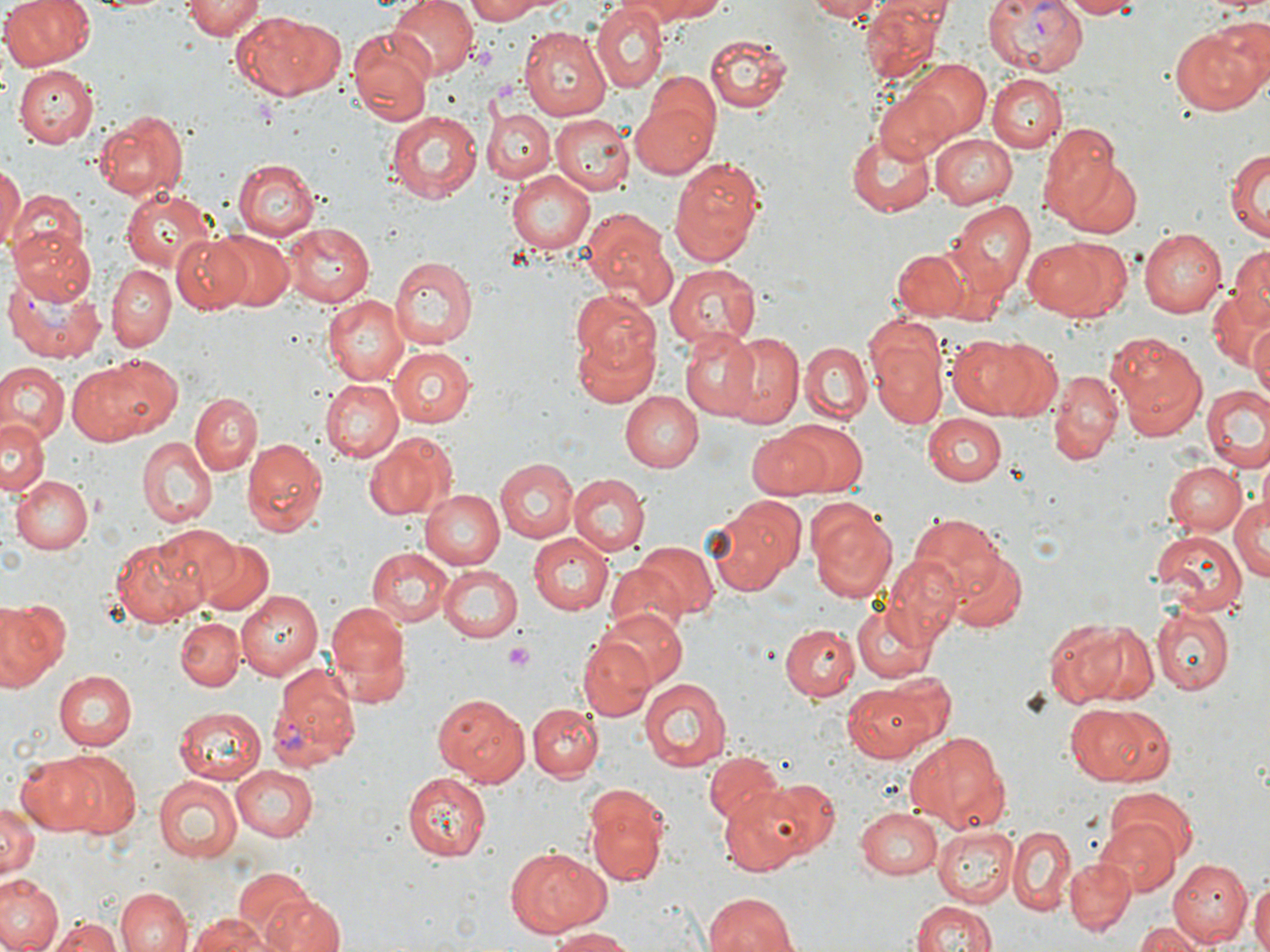
slide-level diagnosis = Plasmodium vivax
platelet locations = approximate bounding boxes as (x1,y1)-(x2,y2) corner pairs in pixels: (471,47)-(496,70), (505,643)-(536,671)
image size = 1270×952 pixels
magnification = 1000x
preparation = thin blood film
stain = May-Grünwald-Giemsa
Plasmodium vivax-infected red blood cell locations = approximate bounding boxes as (x1,y1)-(x2,y2) corner pairs in pixels: (981,0)-(1090,75), (4,269)-(105,363), (265,671)-(362,775)
field of view = one of a larger specimen
modality = optical microscopy
uninfected red blood cell locations = approximate bounding boxes as (x1,y1)-(x2,y2) corner pairs in pixels: (1,0)-(95,70), (179,0)-(263,38), (387,0)-(474,80), (462,0)-(549,24), (615,0)-(726,31), (803,0)-(885,21), (1058,0)-(1142,17), (862,1)-(950,78), (590,5)-(666,89), (230,9)-(345,99), (540,11)-(658,131), (1170,21)-(1267,114), (519,26)-(612,120), (347,29)-(435,127), (704,33)-(791,114), (634,55)-(747,156), (903,59)-(991,142), (12,64)-(98,146), (988,73)-(1065,151), (871,84)-(965,166), (629,93)-(718,178), (483,108)-(554,182), (93,109)-(188,201), (385,112)-(481,203), (551,115)-(633,196), (1039,121)-(1125,224), (847,132)-(936,216), (931,132)-(1018,209), (1224,148)-(1269,242), (1061,156)-(1143,238), (668,159)-(768,267), (0,160)-(23,250), (234,160)-(319,240), (506,170)-(594,254), (120,188)-(216,273), (7,190)-(89,275), (947,201)-(1036,297), (581,209)-(678,311), (283,222)-(374,306), (11,227)-(97,307), (1138,229)-(1226,317), (210,230)-(294,310), (173,232)-(257,315), (1021,238)-(1130,323), (1229,244)-(1270,323), (891,248)-(970,321), (391,257)-(478,349), (104,265)-(174,352), (665,265)-(762,348), (1205,285)-(1267,374), (571,288)-(659,380), (324,296)-(408,387), (1249,323)-(1270,404), (573,327)-(659,408), (679,329)-(764,421), (868,331)-(950,427), (946,332)-(1056,419), (721,333)-(803,425), (1104,333)-(1207,438), (800,341)-(872,423), (390,347)-(475,427), (67,355)-(174,446), (2,362)-(68,444), (1049,372)-(1122,461), (318,378)-(402,462), (1202,385)-(1269,472), (621,391)-(701,472), (191,392)-(262,475), (922,414)-(1005,486), (0,419)-(46,498), (782,422)-(867,494), (746,427)-(832,498), (363,431)-(459,520), (136,437)-(218,529), (243,437)-(328,537), (495,459)-(577,543), (1165,461)-(1246,535), (568,474)-(649,557), (11,475)-(93,554), (423,489)-(505,570), (1230,491)-(1270,585), (703,495)-(804,595), (806,498)-(898,604), (907,510)-(1010,602), (152,525)-(242,605), (529,531)-(614,615), (1152,531)-(1244,616), (111,535)-(205,626), (195,539)-(272,615), (631,541)-(720,621), (367,546)-(451,627), (945,548)-(1026,631), (887,557)-(965,641), (604,561)-(691,639), (438,565)-(524,643), (235,590)-(324,678), (0,596)-(71,692), (853,602)-(940,685), (328,603)-(411,686), (599,606)-(688,689), (1152,608)-(1233,694), (1048,615)-(1157,706), (175,617)-(245,693), (779,623)-(858,701), (580,636)-(653,719), (52,669)-(136,748), (639,677)-(732,773), (845,681)-(945,762), (434,691)-(530,788), (528,702)-(604,779), (1062,702)-(1166,785), (174,706)-(266,783), (907,730)-(1010,832), (706,752)-(786,828), (16,753)-(107,837), (59,754)-(141,836), (230,765)-(318,840), (407,771)-(493,861), (864,772)-(979,872), (153,775)-(243,864), (733,777)-(839,870), (1105,786)-(1199,865), (584,787)-(669,886), (0,798)-(39,877), (856,807)-(942,879), (1093,819)-(1182,895), (934,826)-(1017,906), (1007,828)-(1075,917), (505,846)-(610,935), (1065,857)-(1134,933), (1169,859)-(1250,944), (231,866)-(321,943), (0,875)-(61,952), (1249,875)-(1270,952), (117,888)-(191,952), (702,890)-(799,951), (264,897)-(343,952), (910,898)-(1000,952), (185,913)-(279,952), (52,915)-(125,952), (1135,923)-(1207,951), (548,927)-(635,951)